Name the parasite shown.
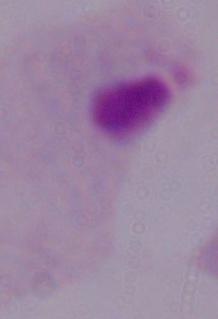

This is a trichomonad.

modality: micrograph
magnification: 1000x